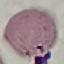
Malaria status: uninfected. Giemsa-stained preparation. Photographed with a smartphone camera at the microscope eyepiece. Thin smear of blood. Automatically extracted cell patch, resized to 64 × 64 pixels.